Locate every malaria parasite.
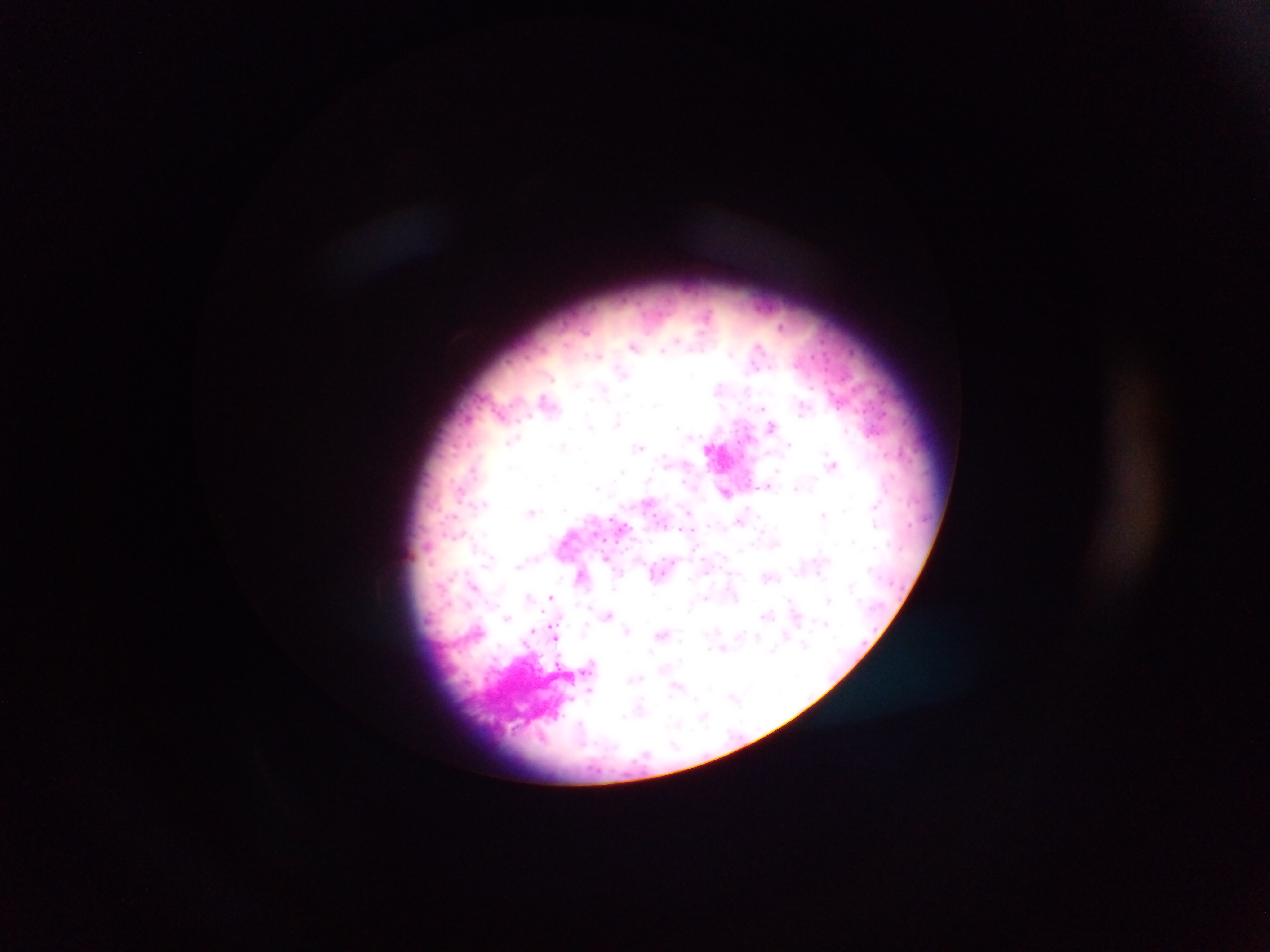
Approximate centers as x y in pixels.
Malaria parasites: 645 316; 675 339; 826 342; 632 345; 663 349; 598 355; 754 361; 796 367; 773 368; 554 381; 544 395; 761 407; 838 407; 883 413; 529 415; 501 416; 519 421; 616 422; 772 425; 678 427; 740 444; 639 448; 885 454; 909 461; 833 464; 472 467; 620 473; 453 479; 683 481; 769 483; 598 490; 690 509; 846 510; 532 512; 823 514; 739 520; 910 524; 681 529; 595 533; 604 539; 619 541; 852 542; 517 566; 581 573; 665 573; 821 575; 476 583; 848 585; 902 587; 528 594; 551 596; 828 600; 766 614; 506 618; 825 624; 629 629; 533 632; 661 633; 756 637; 555 638; 806 644; 723 648; 774 648; 634 677; 589 692; 733 697; 694 700; 706 719; 677 722; 541 735.

capture = mobile-phone photograph through a microscope
preparation = thick blood film
image size = 1270×952 pixels
field of view = single
country = Ghana